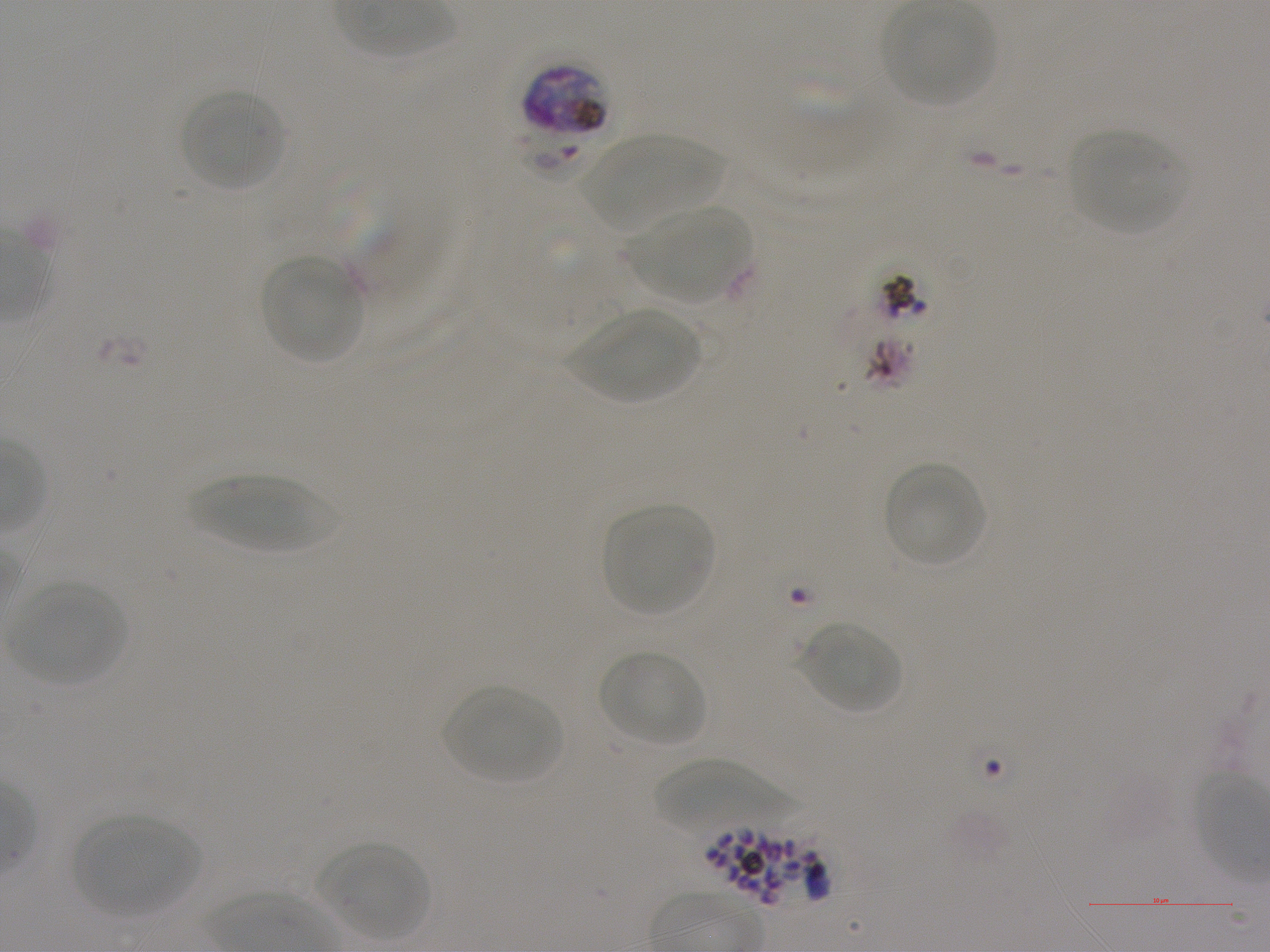
Approximate bounding boxes as [x1, y1, x2, y2] in pixels. Not every red blood cell is marked. A life-cycle stage — or a range of stages, where the recorded stages span more than one — follows each staged infected red blood cell.
Summary:
  - Locations of infected red blood cells: [522, 63, 610, 138] schizont
  - Locations of uninfected red blood cells: [882, 2, 994, 106], [179, 88, 287, 192], [1069, 129, 1188, 235], [579, 134, 722, 230], [348, 191, 466, 342], [626, 205, 751, 300], [260, 254, 364, 363], [568, 308, 700, 401], [882, 461, 988, 568], [186, 475, 339, 553], [602, 504, 714, 616], [9, 582, 126, 685], [799, 621, 902, 714], [597, 649, 708, 747], [441, 684, 563, 785], [649, 758, 803, 834], [73, 814, 204, 914], [318, 842, 430, 941]
  - Donor blood group: A+
  - Preparation: thin blood film
  - Objective: 100x, oil immersion, numerical aperture 1.25
  - Image size: 1270×952 pixels
  - Field of view: single
  - Culture: static in-vitro P. falciparum strain NF54
  - Stain: Giemsa